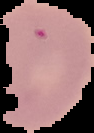

image size = 94×133 pixels
image type = segmented cell region on a black background
malaria status = uninfected
preparation = thin blood smear